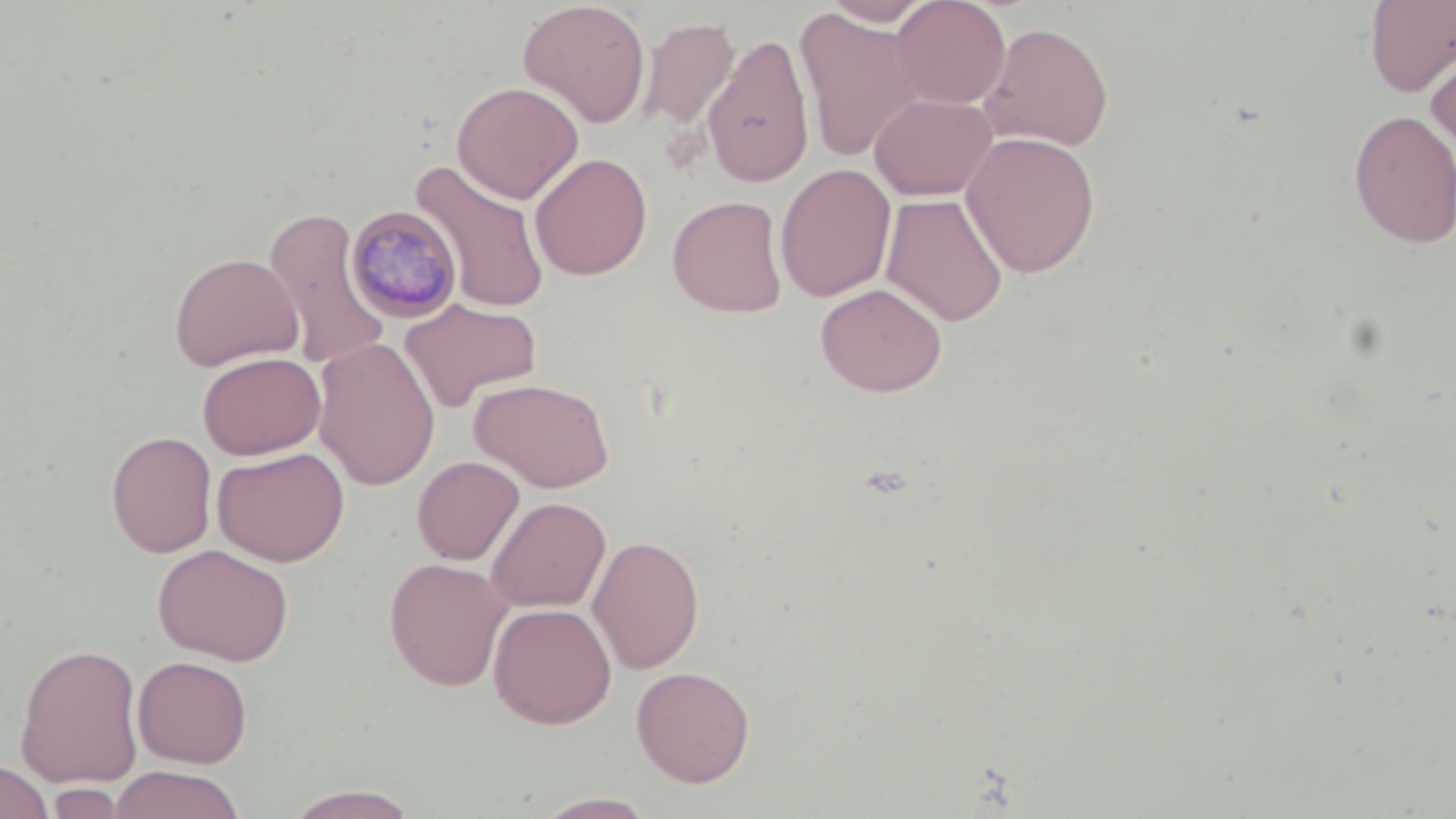

slide-level diagnosis = Plasmodium malariae
magnification = 1000x
stain = May-Grünwald-Giemsa
preparation = thin blood film
uninfected red blood cell locations = approximate bounding boxes as (x1, y1, x2, y2) in pixels: (821, 0, 937, 27), (890, 0, 1012, 109), (1363, 0, 1456, 97), (517, 1, 651, 128), (794, 8, 923, 163), (636, 16, 740, 131), (978, 21, 1114, 151), (701, 34, 815, 188), (1425, 43, 1456, 157), (452, 81, 584, 203), (870, 93, 998, 201), (1348, 110, 1456, 249), (960, 131, 1101, 279), (529, 152, 653, 281), (410, 160, 552, 312), (775, 163, 896, 302), (880, 193, 1009, 327), (666, 194, 789, 317), (262, 207, 392, 372), (168, 252, 303, 371), (815, 282, 948, 397), (398, 297, 542, 413), (312, 337, 440, 490), (197, 352, 326, 459), (469, 377, 615, 492), (106, 430, 217, 558), (212, 446, 349, 567), (411, 455, 525, 565), (486, 496, 610, 613), (587, 534, 705, 675), (152, 544, 294, 665), (384, 557, 513, 692), (488, 603, 616, 728), (14, 642, 145, 788), (132, 655, 253, 767), (631, 665, 756, 788), (0, 759, 54, 819), (107, 766, 246, 819), (47, 784, 128, 819), (281, 784, 423, 818), (533, 792, 658, 818)
Plasmodium malariae-infected red blood cell locations = approximate bounding boxes as (x1, y1, x2, y2) in pixels: (345, 205, 464, 323)
modality = optical microscopy
image size = 1456×819 pixels
field of view = single